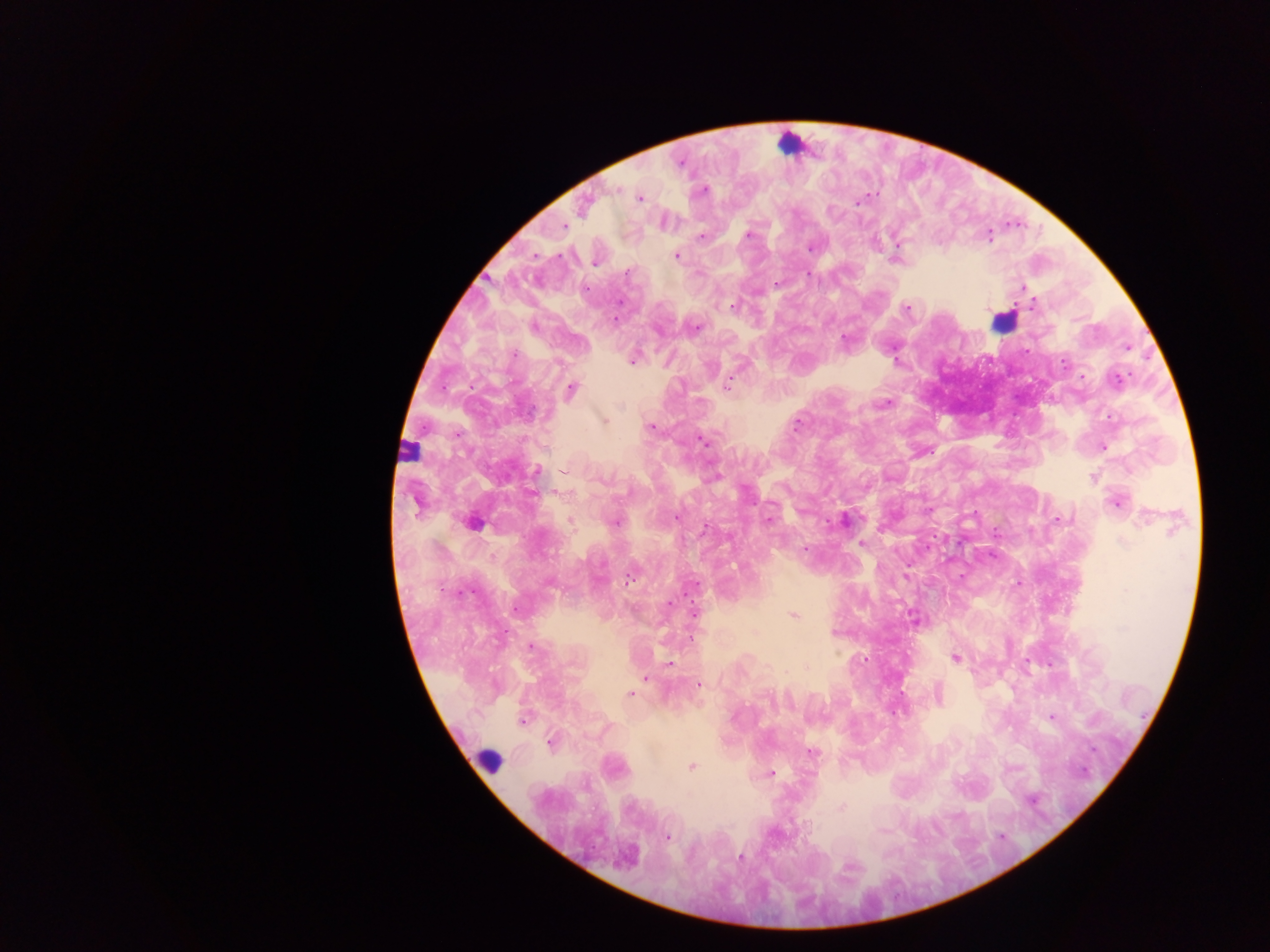
Approximate centers as (x, y) in pixels. Leukocyte locations: (788, 145), (1003, 322), (412, 449), (489, 761). Malaria parasite locations: (617, 190), (704, 190), (639, 198), (857, 201), (584, 204), (565, 226), (749, 235), (701, 236), (989, 236), (811, 248), (676, 255), (536, 256), (594, 263), (627, 273), (807, 274), (776, 284), (1023, 288), (1032, 305), (732, 307), (907, 309), (615, 319), (533, 326), (696, 327), (844, 339), (514, 355), (633, 362), (1063, 363), (1083, 376), (1117, 380), (727, 387), (571, 390), (887, 403), (604, 421), (796, 425), (651, 426), (704, 442), (1103, 447), (537, 470), (1092, 478), (532, 493), (1116, 502), (415, 505), (676, 517), (1145, 518), (844, 519), (1060, 519), (571, 521), (768, 521), (616, 522), (472, 523), (706, 528), (1123, 542), (861, 544), (804, 549), (628, 581), (550, 584), (696, 584), (668, 603), (516, 610), (694, 613), (793, 616), (834, 633), (532, 647), (955, 658), (669, 663), (806, 667), (645, 678), (699, 685), (630, 695), (938, 696), (1052, 717), (522, 721), (550, 743), (811, 753), (691, 767), (771, 773), (841, 808), (667, 837), (741, 857), (627, 859), (848, 868). Collected in Ghana. One field of view. Image is 1270×952 pixels. Mobile-phone photograph taken through the microscope. Thick blood smear.